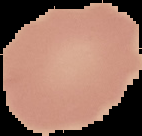

Malaria status: uninfected. Image is 142×136 pixels. The area outside the segmented cell region is set to black. From a thin blood smear.